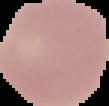

preparation = thin blood film
image size = 109×106 pixels
image type = segmented cell region on a black background
malaria status = uninfected